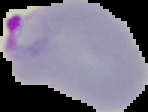
Image is 148×112 pixels. Malaria status: parasitized. Cell region segmented out of the field of view; the surrounding area is masked to black. From a thin blood smear.